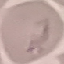

malaria status = uninfected
stain = Giemsa
capture = smartphone through the microscope eyepiece
image type = cell patch, automatically extracted from a larger field of view and resized to 64 × 64 pixels
preparation = thin blood film